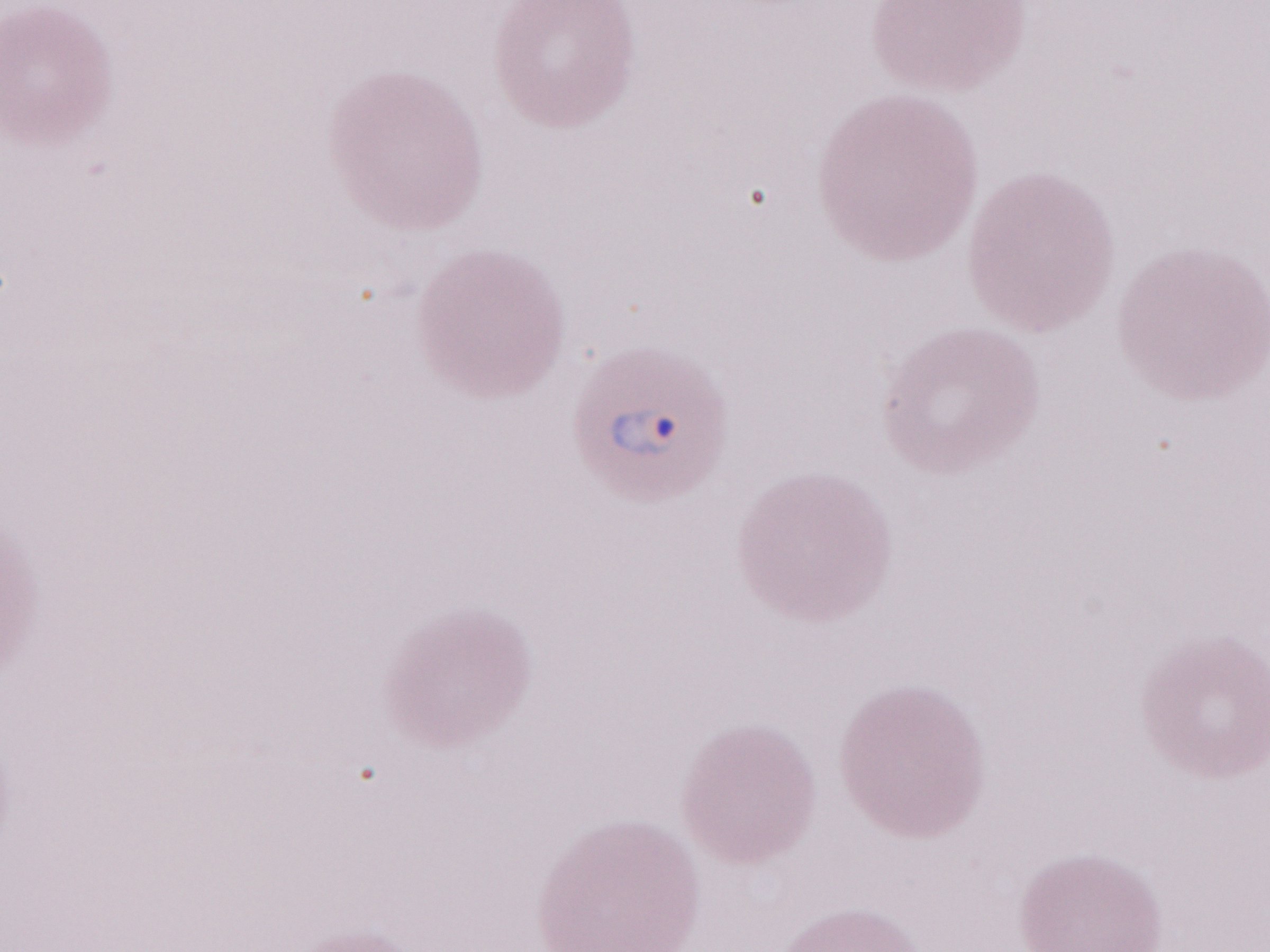 Image is 1270×952 pixels. 1,000x magnification. Thin blood film. Malaria diagnosis (patient-level): positive. One field of this slide. May-Grünwald-Giemsa (MGG) stain. Olympus BX43 microscope, Olympus DP73 camera.